Assess this cell for malaria.
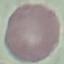

Uninfected.

Photographed with a smartphone camera at the microscope eyepiece. Giemsa-stained preparation. Cell patch, automatically extracted from a larger field of view and resized to 64 × 64 pixels. Thin blood smear.